Locate and identify every blood parasite.
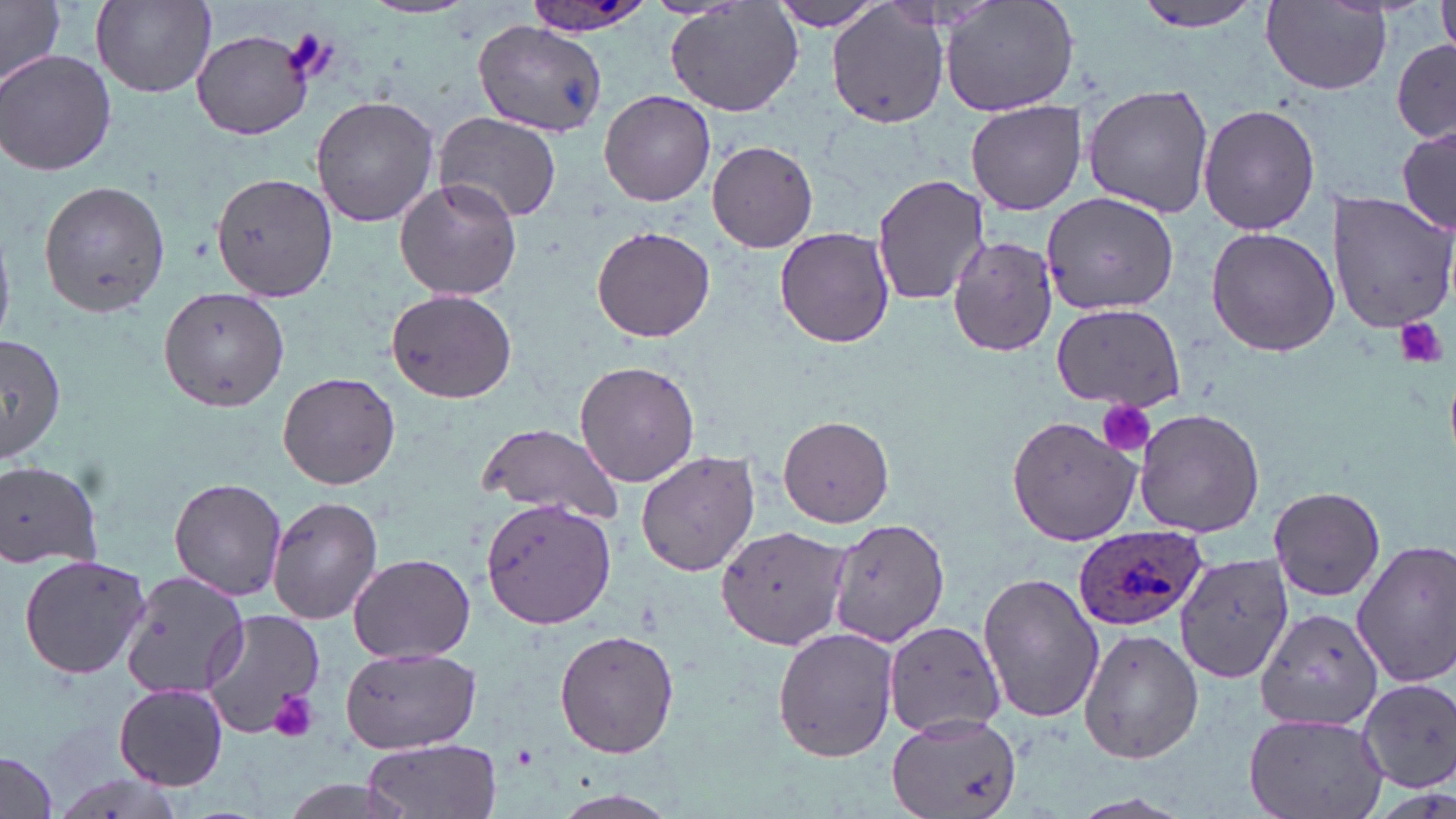

Approximate bounding boxes as named x1/y1/x2/y2 corners in pixels.
Plasmodium ovale-infected red blood cells: (x1=520, y1=0, x2=657, y2=39), (x1=1071, y1=526, x2=1205, y2=632).
No Plasmodium falciparum, Plasmodium malariae, Plasmodium vivax, Babesia divergens, or Trypanosoma brucei observed.

{
  "slide_level_diagnosis": "Plasmodium ovale",
  "preparation": "thin blood film",
  "image_size": "1456×819 pixels",
  "stain": "May-Grünwald-Giemsa",
  "field_of_view": "one of a larger specimen",
  "modality": "optical microscopy",
  "magnification": "1000x",
  "uninfected_red_blood_cell_locations": "approximate bounding boxes as named x1/y1/x2/y2 corners in pixels: (x1=0, y1=0, x2=65, y2=92), (x1=91, y1=0, x2=215, y2=96), (x1=665, y1=0, x2=806, y2=118), (x1=765, y1=0, x2=893, y2=31), (x1=940, y1=0, x2=1078, y2=115), (x1=1129, y1=0, x2=1271, y2=36), (x1=1439, y1=0, x2=1456, y2=59), (x1=827, y1=2, x2=948, y2=130), (x1=1262, y1=2, x2=1393, y2=93), (x1=475, y1=19, x2=606, y2=138), (x1=192, y1=29, x2=312, y2=139), (x1=1392, y1=38, x2=1455, y2=145), (x1=2, y1=50, x2=118, y2=177), (x1=1081, y1=86, x2=1214, y2=218), (x1=598, y1=90, x2=716, y2=207), (x1=310, y1=95, x2=440, y2=228), (x1=966, y1=100, x2=1088, y2=216), (x1=1199, y1=102, x2=1321, y2=236), (x1=437, y1=111, x2=562, y2=222), (x1=1396, y1=124, x2=1456, y2=236), (x1=706, y1=140, x2=819, y2=253), (x1=212, y1=171, x2=338, y2=301), (x1=872, y1=173, x2=991, y2=306), (x1=394, y1=177, x2=521, y2=301), (x1=38, y1=179, x2=171, y2=316), (x1=1043, y1=189, x2=1180, y2=314), (x1=1328, y1=192, x2=1456, y2=333), (x1=592, y1=225, x2=715, y2=343), (x1=775, y1=226, x2=895, y2=349), (x1=1205, y1=226, x2=1340, y2=357), (x1=946, y1=235, x2=1059, y2=356), (x1=157, y1=286, x2=291, y2=411), (x1=388, y1=289, x2=519, y2=402), (x1=1051, y1=303, x2=1184, y2=409), (x1=0, y1=335, x2=68, y2=461), (x1=574, y1=359, x2=700, y2=488), (x1=277, y1=371, x2=401, y2=491), (x1=1133, y1=406, x2=1265, y2=537), (x1=779, y1=414, x2=893, y2=528), (x1=1006, y1=416, x2=1138, y2=546), (x1=478, y1=420, x2=625, y2=525), (x1=634, y1=450, x2=761, y2=577), (x1=0, y1=458, x2=106, y2=569), (x1=168, y1=478, x2=289, y2=603), (x1=1268, y1=485, x2=1387, y2=603), (x1=268, y1=494, x2=385, y2=625), (x1=479, y1=497, x2=618, y2=630), (x1=830, y1=518, x2=950, y2=645), (x1=718, y1=524, x2=846, y2=650), (x1=1352, y1=539, x2=1456, y2=688), (x1=1173, y1=550, x2=1295, y2=684), (x1=347, y1=551, x2=475, y2=662), (x1=18, y1=553, x2=152, y2=682), (x1=118, y1=571, x2=251, y2=699), (x1=978, y1=571, x2=1103, y2=723), (x1=200, y1=608, x2=330, y2=737), (x1=1257, y1=609, x2=1383, y2=732), (x1=883, y1=619, x2=1005, y2=739), (x1=772, y1=625, x2=897, y2=762), (x1=1079, y1=627, x2=1206, y2=763), (x1=554, y1=629, x2=681, y2=759), (x1=338, y1=647, x2=481, y2=752), (x1=1356, y1=679, x2=1455, y2=792), (x1=114, y1=683, x2=228, y2=788), (x1=1242, y1=712, x2=1390, y2=819), (x1=885, y1=713, x2=1022, y2=819), (x1=365, y1=737, x2=500, y2=819), (x1=0, y1=750, x2=59, y2=819), (x1=545, y1=789, x2=684, y2=819)",
  "platelet_locations": "approximate bounding boxes as named x1/y1/x2/y2 corners in pixels: (x1=283, y1=26, x2=337, y2=85), (x1=1396, y1=316, x2=1447, y2=368), (x1=1093, y1=397, x2=1157, y2=459), (x1=268, y1=690, x2=319, y2=741)"
}